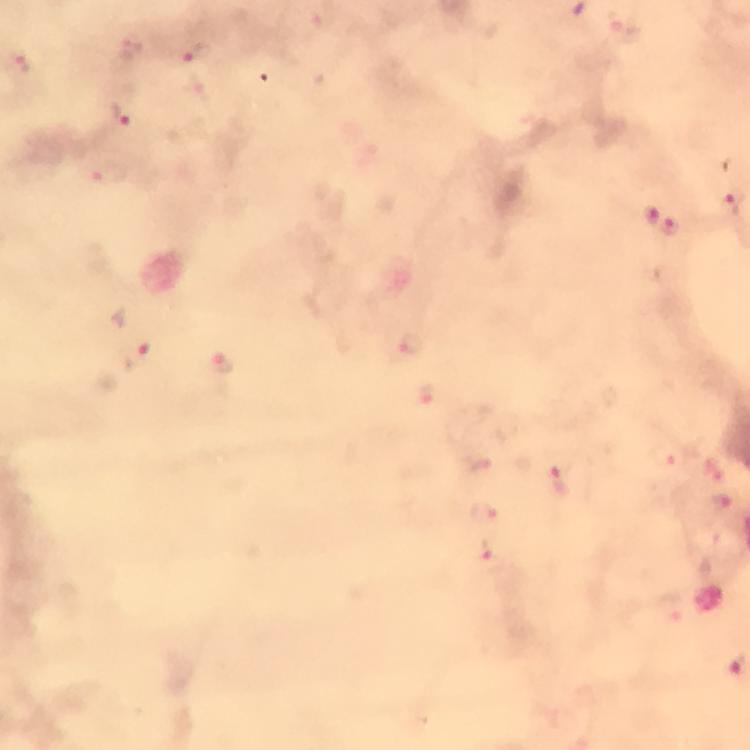
Approximate centers as [x, y] in pixels.
Summary:
  - Malaria parasite locations: [199, 53], [23, 62], [123, 116], [734, 204], [649, 216], [671, 226], [413, 344], [136, 359], [227, 371], [425, 395], [560, 480], [483, 515], [483, 551], [739, 664]
  - Stain: Giemsa
  - Context: from a diagnostic examination for malaria
  - Capture: smartphone camera through the microscope
  - Magnification: 100x
  - Preparation: thick smear
  - Cropped from: a single field of view
  - Image size: 750×750 pixels
  - Immersion oil: applied